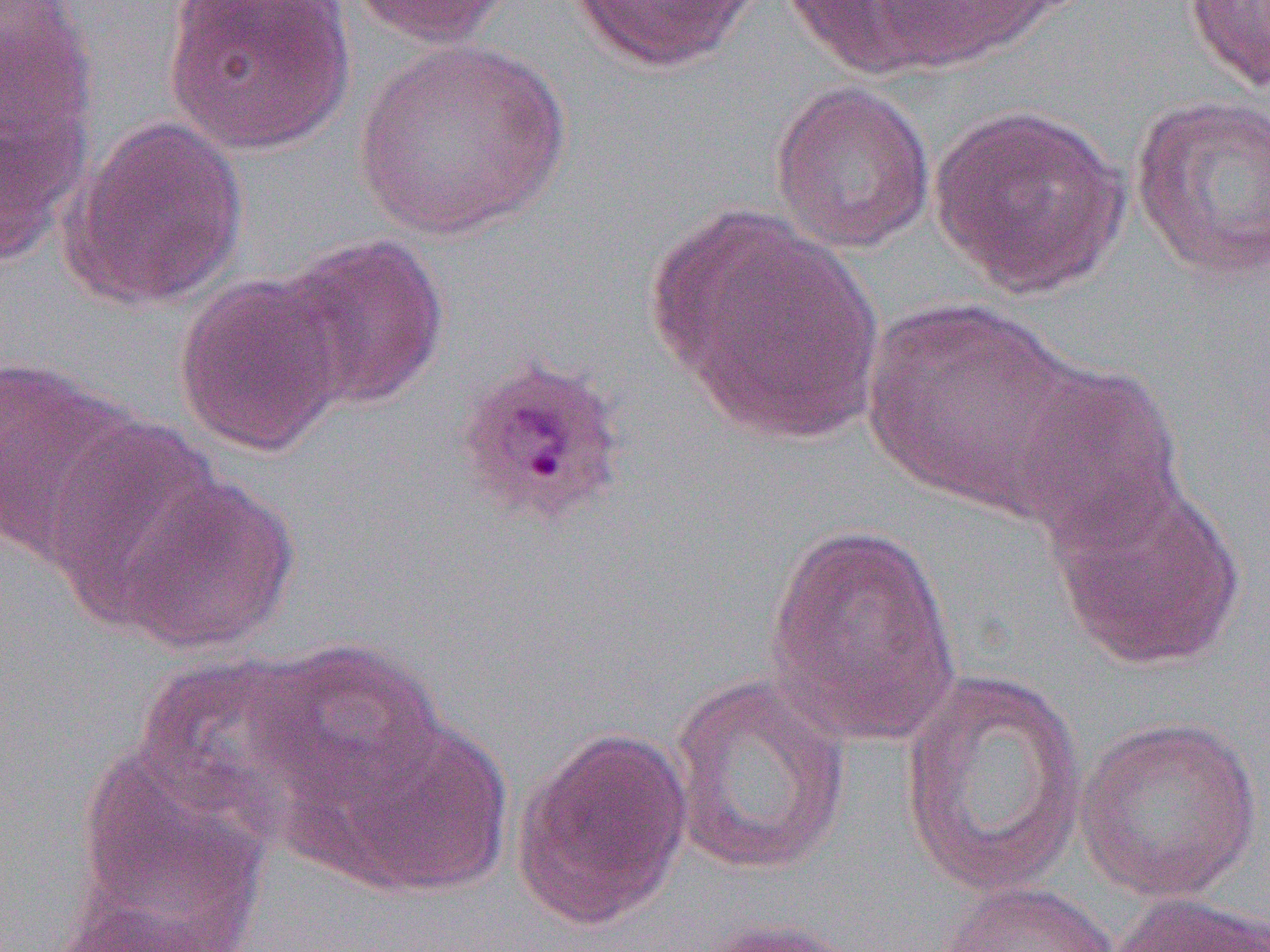

Summary:
  - Coordinate format: approximate bounding boxes as [x1, y1, x2, y2] in pixels
  - Plasmodium ovale-infected red blood cell locations: [451, 353, 631, 531]
  - Uninfected red blood cell locations: [0, 0, 97, 155], [163, 0, 355, 156], [349, 0, 516, 48], [567, 0, 765, 72], [781, 0, 959, 80], [866, 0, 1059, 72], [1182, 0, 1270, 94], [352, 38, 570, 241], [768, 80, 936, 255], [0, 89, 90, 265], [1130, 93, 1270, 282], [928, 101, 1130, 299], [62, 116, 250, 312], [655, 209, 886, 445], [274, 232, 451, 411], [172, 272, 348, 458], [861, 298, 1083, 513], [0, 356, 141, 564], [1008, 359, 1188, 554], [39, 418, 225, 623], [113, 472, 300, 655], [1048, 476, 1248, 672], [765, 523, 963, 746], [246, 637, 447, 808], [132, 653, 334, 839], [900, 668, 1090, 897], [666, 672, 853, 877], [324, 713, 514, 897], [1075, 714, 1264, 901], [512, 724, 694, 933], [66, 747, 271, 944], [937, 881, 1121, 952], [1106, 891, 1270, 952], [694, 918, 873, 951]
  - Slide-level diagnosis: Plasmodium ovale
  - Modality: light microscopy
  - Preparation: thin blood film
  - Image size: 1270×952 pixels
  - Field of view: one of a larger specimen
  - Magnification: 1000x